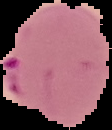
From a thin blood film. The area outside the segmented cell region is set to black. Image is 112×130 pixels. Malaria status: parasitized.